Give the extent of all Trypanosoma brucei.
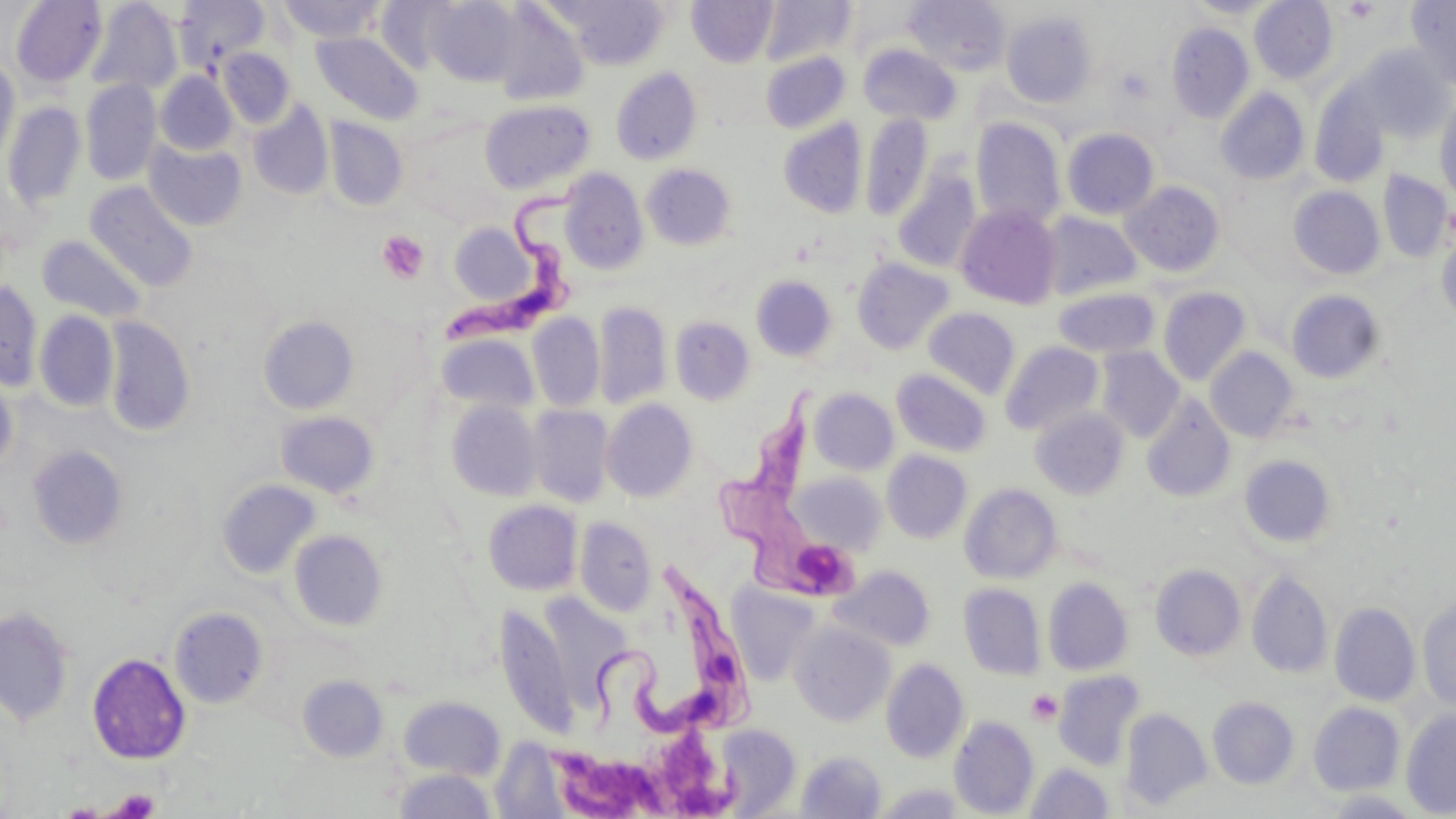

Approximate bounding boxes as (x1,y1)-(x2,y2) corner pairs in pixels.
Trypanosoma brucei: (444,175)-(589,347), (717,371)-(866,612), (580,550)-(761,743).

Summary:
  - Uninfected red blood cell locations: (11,0)-(107,87), (276,0)-(387,42), (424,0)-(521,86), (552,0)-(669,70), (687,0)-(777,67), (760,0)-(855,66), (905,0)-(1011,77), (1186,0)-(1279,18), (1249,0)-(1338,85), (1406,0)-(1456,90), (87,1)-(182,96), (174,1)-(269,71), (375,1)-(457,73), (490,3)-(589,107), (1001,11)-(1097,107), (1167,22)-(1254,123), (312,31)-(423,125), (858,44)-(960,125), (1354,45)-(1455,142), (217,47)-(295,129), (760,52)-(850,133), (0,55)-(21,167), (610,68)-(702,165), (155,72)-(237,155), (80,79)-(161,185), (1309,85)-(1390,188), (1216,87)-(1310,185), (1435,96)-(1456,203), (480,100)-(594,194), (3,101)-(87,211), (248,101)-(333,200), (861,114)-(933,222), (324,118)-(408,211), (970,118)-(1066,229), (778,119)-(867,218), (1061,128)-(1160,220), (144,139)-(248,231), (642,164)-(736,250), (560,170)-(649,274), (1378,170)-(1452,263), (893,171)-(980,273), (1121,180)-(1226,277), (85,181)-(199,292), (1288,186)-(1385,279), (956,204)-(1062,309), (1038,212)-(1143,301), (448,222)-(538,306), (1437,229)-(1456,326), (37,235)-(148,323), (852,257)-(955,355), (751,275)-(836,362), (0,281)-(43,391), (1052,287)-(1161,359), (1158,287)-(1251,386), (1286,289)-(1386,384), (594,301)-(672,409), (923,307)-(1020,399), (34,310)-(119,412), (528,313)-(604,411), (259,315)-(359,414), (102,316)-(196,437), (670,317)-(755,405), (437,333)-(539,414), (1000,341)-(1104,436), (1096,347)-(1184,442), (1205,347)-(1298,442), (891,368)-(992,457), (0,373)-(18,477), (809,388)-(899,475), (1142,394)-(1236,502), (445,400)-(543,502), (602,400)-(697,502), (527,405)-(614,508), (1030,407)-(1130,499), (275,411)-(380,499), (27,445)-(128,549), (882,451)-(972,543), (1239,454)-(1337,549), (797,475)-(886,554), (217,478)-(321,579), (960,484)-(1062,583), (483,500)-(582,596), (575,517)-(657,616), (289,528)-(389,631), (1150,563)-(1246,658), (830,565)-(936,652), (1247,571)-(1333,678), (1043,578)-(1133,675), (726,583)-(823,688), (959,583)-(1046,680), (546,592)-(630,706), (1418,597)-(1456,710), (495,603)-(576,738), (1330,603)-(1420,706), (0,606)-(75,726), (169,606)-(269,708), (789,622)-(895,727), (87,652)-(191,764), (881,658)-(969,764), (1054,670)-(1145,771), (297,675)-(389,761), (398,695)-(506,781), (1208,697)-(1299,789), (1308,702)-(1405,795), (1121,708)-(1212,811), (1401,708)-(1456,817), (949,716)-(1039,817), (713,724)-(801,816), (491,739)-(572,817), (795,750)-(887,818), (1026,762)-(1114,818), (393,768)-(498,818), (873,783)-(967,818)
  - Platelet locations: (1344,1)-(1380,22), (377,230)-(429,284), (1026,689)-(1063,726), (658,726)-(717,812), (550,747)-(645,819), (107,788)-(161,818)
  - Slide-level diagnosis: Trypanosoma brucei
  - Modality: optical microscopy
  - Preparation: thin blood film
  - Field of view: single
  - Image size: 1456×819 pixels
  - Stain: May-Grünwald-Giemsa
  - Magnification: 1000x